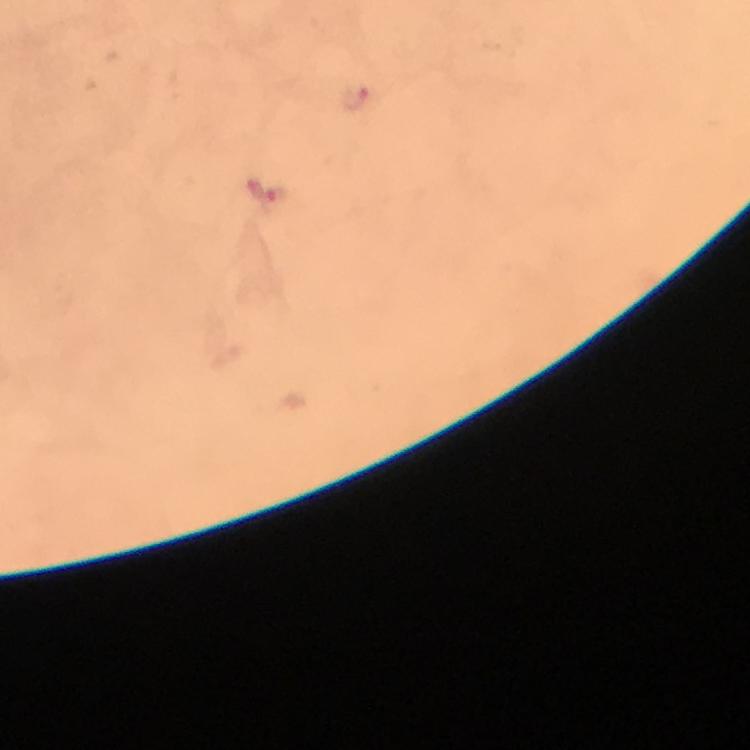
plasmodium_parasite_locations: 'approximate centers as {x, y} in pixels: {356, 100}, {270, 195}'
preparation: thick blood film
cropped_from: a single field of view
context: from a diagnostic examination for malaria
stain: Giemsa
immersion_oil: applied
capture: smartphone camera through the microscope
magnification: 100x
image_size: 750×750 pixels